Locate the cells, classifying each as a parasitized red blood cell, an uninfected red blood cell, or a white blood cell.
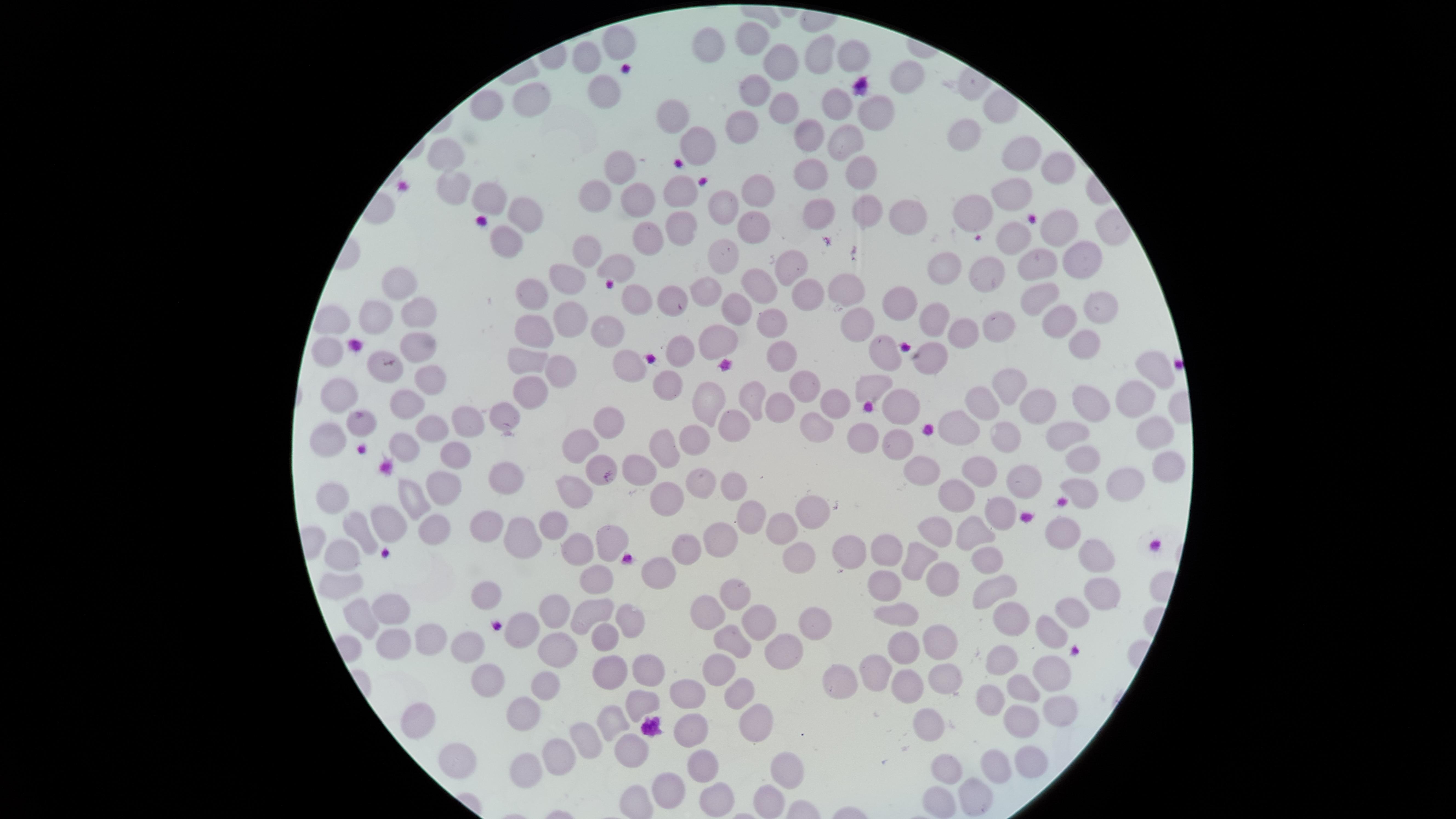

No parasitized red blood cells identified.
Approximate marker points, in pixels from the top-left corner.
Uninfected red blood cells: (x=756, y=36), (x=713, y=39), (x=617, y=44), (x=848, y=51), (x=820, y=55), (x=586, y=58), (x=786, y=61), (x=908, y=76), (x=756, y=88), (x=611, y=89), (x=536, y=98), (x=492, y=103), (x=835, y=104), (x=790, y=105), (x=874, y=107), (x=674, y=113), (x=743, y=121), (x=965, y=132), (x=810, y=139), (x=848, y=141), (x=701, y=149), (x=1027, y=151), (x=449, y=156), (x=1056, y=166), (x=622, y=168), (x=865, y=170), (x=813, y=171), (x=454, y=185), (x=681, y=192), (x=760, y=192), (x=1010, y=192), (x=491, y=194), (x=633, y=198), (x=600, y=200), (x=976, y=208), (x=727, y=211), (x=868, y=213), (x=526, y=214), (x=902, y=214), (x=823, y=215), (x=686, y=222), (x=1061, y=226), (x=757, y=227), (x=1017, y=230), (x=647, y=234), (x=501, y=243), (x=727, y=250), (x=589, y=251), (x=1044, y=260), (x=1083, y=261), (x=621, y=265), (x=791, y=266), (x=945, y=266), (x=985, y=269), (x=568, y=273), (x=844, y=280), (x=398, y=285), (x=711, y=285), (x=758, y=289), (x=537, y=291), (x=1046, y=291), (x=808, y=294), (x=638, y=296), (x=673, y=298), (x=902, y=299), (x=1106, y=303), (x=737, y=304), (x=414, y=312), (x=942, y=318), (x=1063, y=318), (x=331, y=319), (x=377, y=319), (x=575, y=319), (x=774, y=320), (x=857, y=321), (x=1006, y=324), (x=535, y=326), (x=969, y=326), (x=608, y=329), (x=716, y=337), (x=1091, y=341), (x=680, y=345), (x=416, y=350), (x=329, y=351), (x=883, y=352), (x=930, y=352), (x=778, y=355), (x=529, y=361), (x=628, y=363), (x=1153, y=363), (x=567, y=370), (x=387, y=371), (x=429, y=380), (x=801, y=381), (x=869, y=381), (x=667, y=382), (x=1009, y=386), (x=340, y=390), (x=531, y=391), (x=750, y=393), (x=707, y=398), (x=1134, y=398), (x=988, y=401), (x=1093, y=401), (x=907, y=402), (x=407, y=403), (x=1046, y=404), (x=839, y=405), (x=780, y=406), (x=466, y=410), (x=503, y=411), (x=961, y=416), (x=366, y=418), (x=609, y=422), (x=817, y=422), (x=431, y=423), (x=730, y=423), (x=1065, y=424), (x=330, y=431), (x=1158, y=431), (x=860, y=436), (x=580, y=440), (x=1007, y=440), (x=699, y=442), (x=404, y=445), (x=660, y=446), (x=900, y=446), (x=1089, y=451), (x=455, y=452), (x=641, y=462), (x=594, y=466), (x=923, y=468), (x=1165, y=469), (x=977, y=472), (x=504, y=474), (x=1127, y=477), (x=703, y=479), (x=1033, y=479), (x=443, y=482), (x=731, y=485), (x=1082, y=487), (x=958, y=489), (x=572, y=490), (x=671, y=493), (x=404, y=496), (x=333, y=497), (x=1002, y=511), (x=810, y=513), (x=743, y=516), (x=490, y=517), (x=553, y=522), (x=379, y=525), (x=980, y=527), (x=431, y=528), (x=785, y=528), (x=934, y=528), (x=1061, y=529), (x=359, y=533), (x=720, y=536), (x=523, y=537), (x=604, y=539), (x=883, y=546), (x=577, y=548), (x=844, y=548), (x=684, y=549), (x=343, y=553), (x=921, y=558), (x=989, y=558), (x=800, y=559), (x=1098, y=559), (x=593, y=573), (x=658, y=578), (x=939, y=579), (x=884, y=584), (x=332, y=585), (x=1000, y=585), (x=736, y=587), (x=1102, y=591), (x=489, y=597), (x=706, y=606), (x=592, y=607), (x=391, y=608), (x=556, y=608), (x=896, y=610), (x=1067, y=613), (x=1010, y=614), (x=365, y=615), (x=761, y=618), (x=636, y=619), (x=812, y=623), (x=521, y=628), (x=1049, y=632), (x=431, y=635), (x=731, y=635), (x=606, y=636), (x=395, y=643), (x=938, y=643), (x=464, y=644), (x=905, y=646), (x=560, y=649), (x=779, y=650), (x=648, y=662), (x=1005, y=662), (x=882, y=665), (x=718, y=668), (x=944, y=671), (x=1056, y=671), (x=610, y=672), (x=840, y=676), (x=914, y=676), (x=491, y=677), (x=540, y=682), (x=1021, y=685), (x=692, y=692), (x=743, y=692), (x=992, y=699), (x=638, y=702), (x=1060, y=708), (x=523, y=710), (x=423, y=714), (x=612, y=719), (x=755, y=720), (x=928, y=721), (x=1029, y=724), (x=694, y=727), (x=587, y=736), (x=631, y=746), (x=457, y=754), (x=555, y=757), (x=1027, y=763), (x=703, y=767), (x=522, y=768), (x=989, y=768), (x=947, y=769), (x=787, y=771), (x=666, y=789), (x=972, y=796), (x=713, y=798), (x=937, y=800), (x=766, y=803).
No white blood cells identified.

preparation = thin smear of blood
image size = 1456×819 pixels
capture = smartphone photograph through the microscope eyepiece
field of view = single
stain = Giemsa
visible region = circular